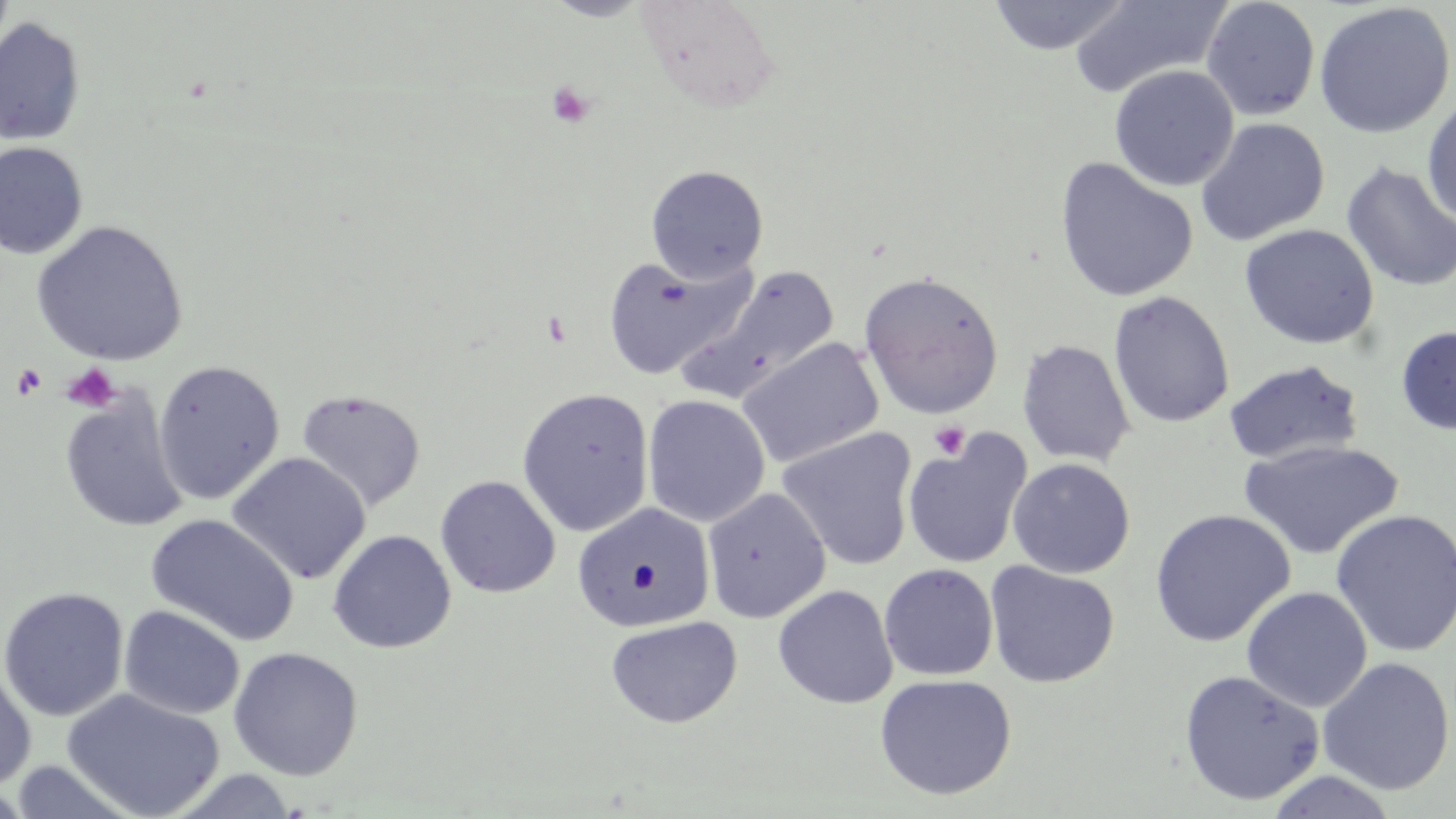

Summary:
  - Coordinate format: approximate bounding boxes as [x1, y1, x2, y2] in pixels
  - Platelet locations: [546, 82, 595, 128], [61, 363, 122, 412], [12, 364, 46, 401], [928, 421, 970, 460]
  - Uninfected red blood cell locations: [0, 0, 16, 67], [544, 0, 654, 21], [636, 0, 780, 110], [985, 0, 1134, 55], [1201, 0, 1321, 121], [1067, 1, 1230, 98], [1313, 2, 1454, 139], [0, 17, 86, 146], [1109, 64, 1239, 191], [1421, 90, 1456, 230], [1195, 118, 1330, 247], [0, 142, 88, 260], [1054, 158, 1198, 303], [1340, 161, 1456, 293], [645, 165, 768, 284], [31, 220, 188, 366], [1239, 223, 1380, 350], [601, 253, 755, 380], [682, 267, 840, 404], [859, 271, 1004, 419], [1108, 290, 1235, 428], [1396, 325, 1456, 435], [736, 337, 885, 469], [1017, 339, 1135, 467], [152, 359, 286, 505], [1222, 359, 1367, 465], [294, 387, 426, 511], [516, 387, 655, 537], [59, 390, 189, 533], [642, 394, 770, 527], [777, 427, 919, 571], [902, 430, 1033, 570], [1238, 439, 1404, 561], [226, 452, 371, 585], [1007, 458, 1135, 578], [435, 475, 560, 598], [702, 487, 831, 623], [571, 502, 715, 633], [1149, 509, 1296, 647], [1329, 509, 1456, 658], [146, 514, 299, 646], [328, 529, 456, 654], [983, 561, 1120, 688], [879, 563, 999, 682], [772, 585, 898, 708], [0, 586, 129, 721], [1241, 586, 1372, 712], [119, 605, 245, 721], [605, 615, 743, 728], [228, 647, 363, 780], [1317, 656, 1455, 795], [0, 662, 36, 790], [1178, 669, 1325, 807], [874, 674, 1017, 801], [60, 689, 225, 819], [8, 760, 140, 819], [164, 769, 302, 818], [1263, 770, 1399, 818]
  - Slide-level diagnosis: no evidence of blood parasites
  - Magnification: 1000x
  - Preparation: thin blood film
  - Image size: 1456×819 pixels
  - Stain: May-Grünwald-Giemsa
  - Field of view: single
  - Modality: light microscopy